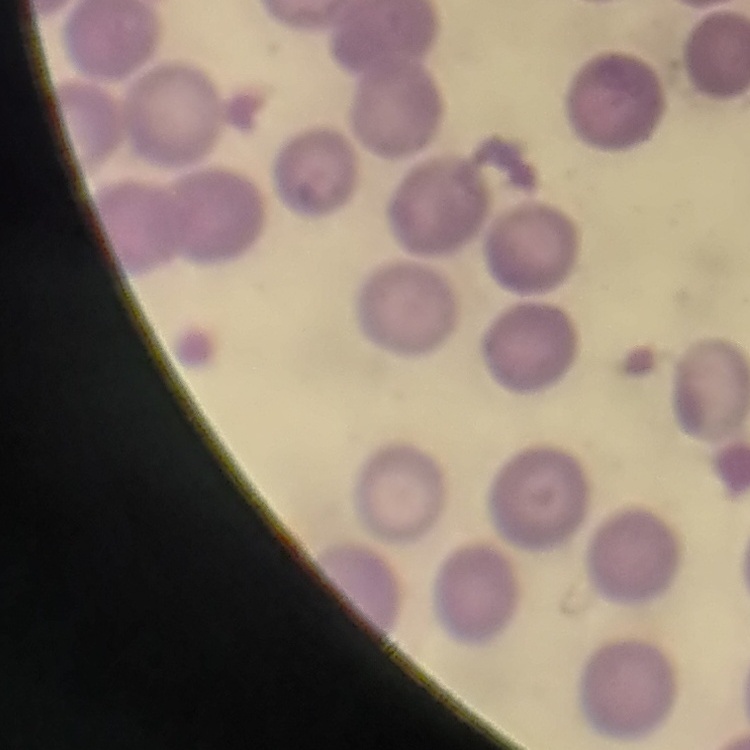
The red blood cells show no rouleaux formation. Thin blood film. One tile cut from a larger photomicrograph. Stained with either Field's or Giemsa.